Classify this cell by malaria status.
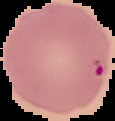
Uninfected.

From a thin blood smear. Image is 115×121 pixels. The area outside the segmented cell region is set to black.